Identify the parasite.
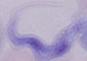

A trypanosome.

Micrograph. Captured at 1000x magnification.